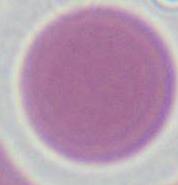

Micrograph. 1000x magnification. A red blood cell is seen.